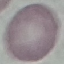

malaria_status: uninfected
image_type: cell patch, automatically extracted from a larger field of view and resized to 64 × 64 pixels
stain: Giemsa
preparation: thin blood film
capture: smartphone camera at the microscope eyepiece